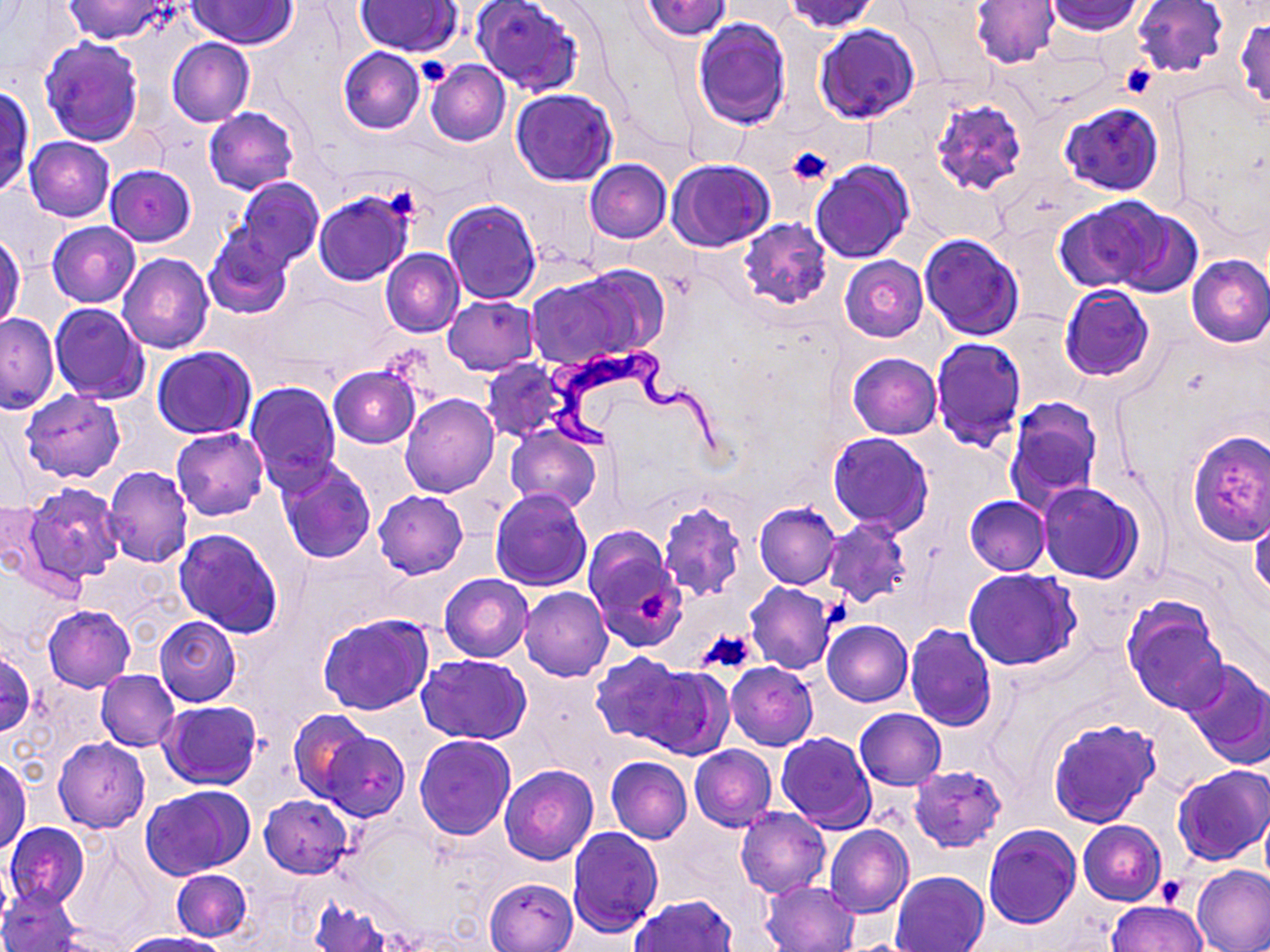
Approximate bounding boxes as (x1,y1)-(x2,y2) corner pairs in pixels. Trypanosoma brucei locations: (539,349)-(733,464). Platelet locations: (414,56)-(455,86), (1119,64)-(1156,97), (786,147)-(831,185), (377,186)-(421,225), (636,590)-(669,622), (698,628)-(760,675), (1154,877)-(1187,907). Uninfected red blood cell locations: (64,0)-(169,44), (188,0)-(297,48), (355,0)-(461,56), (473,0)-(584,96), (642,0)-(730,41), (783,0)-(881,34), (1133,0)-(1229,77), (971,1)-(1058,69), (1044,1)-(1144,35), (1236,16)-(1269,113), (691,17)-(792,129), (813,24)-(920,125), (40,36)-(143,146), (167,38)-(254,127), (338,47)-(425,134), (401,54)-(460,91), (425,59)-(510,146), (1,88)-(32,194), (511,88)-(618,187), (928,92)-(1030,197), (1060,100)-(1163,197), (203,107)-(298,195), (25,136)-(114,221), (667,158)-(775,251), (585,160)-(672,243), (810,160)-(913,263), (104,164)-(196,246), (232,178)-(325,268), (313,191)-(413,284), (442,200)-(542,305), (1052,201)-(1157,292), (1097,203)-(1202,298), (738,217)-(830,309), (47,222)-(140,308), (204,228)-(294,319), (0,231)-(24,332), (919,233)-(1025,339), (380,249)-(465,337), (118,254)-(212,354), (1186,254)-(1269,348), (839,256)-(929,342), (525,269)-(660,372), (1060,284)-(1155,382), (442,295)-(539,375), (50,303)-(150,404), (0,313)-(59,413), (930,337)-(1027,451), (152,346)-(257,439), (847,353)-(941,439), (481,358)-(571,443), (328,366)-(421,448), (245,381)-(341,491), (21,389)-(125,482), (401,396)-(498,498), (1005,397)-(1103,510), (505,426)-(601,515), (172,428)-(267,519), (1186,430)-(1270,544), (828,432)-(934,535), (275,458)-(378,565), (102,466)-(193,567), (1036,482)-(1144,584), (23,483)-(125,586), (490,488)-(592,590), (374,491)-(468,579), (964,496)-(1050,575), (657,499)-(747,601), (0,500)-(49,580), (754,501)-(842,589), (1248,508)-(1270,605), (822,517)-(912,607), (173,527)-(284,638), (583,530)-(687,653), (964,569)-(1082,672), (440,573)-(532,662), (745,583)-(835,674), (519,586)-(612,681), (1124,598)-(1229,715), (43,604)-(135,692), (317,612)-(432,715), (155,617)-(241,706), (823,620)-(913,706), (905,621)-(996,732), (0,649)-(36,736), (591,652)-(695,747), (417,654)-(530,744), (1181,658)-(1270,768), (726,662)-(817,749), (637,664)-(733,759), (96,670)-(179,750), (161,700)-(260,789), (855,708)-(945,790), (290,709)-(378,803), (1047,718)-(1160,827), (315,729)-(410,821), (775,732)-(876,834), (414,733)-(516,839), (54,738)-(150,832), (689,745)-(777,831), (0,755)-(31,852), (605,756)-(692,843), (500,765)-(598,864), (910,765)-(1006,851), (1172,765)-(1269,867), (143,786)-(252,879), (259,795)-(352,878), (735,806)-(830,898), (1079,821)-(1166,905), (4,823)-(89,909), (826,824)-(912,919), (984,824)-(1081,928), (568,827)-(663,935), (1191,866)-(1270,952), (172,868)-(251,942), (890,871)-(990,952), (484,877)-(578,952), (760,880)-(860,951), (0,888)-(82,952), (629,894)-(738,952), (309,898)-(392,951), (1106,900)-(1207,952), (119,933)-(229,952). Slide-level diagnosis: Trypanosoma brucei. One field of a larger specimen. Image is 1270×952 pixels. Thin blood smear. May-Grünwald-Giemsa stain. Light microscopy. Captured at 1000x magnification.